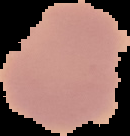
Malaria status: uninfected. From a thin blood smear. Image is 130×136 pixels. Segmented cell region on a black background.